Outline each Trypanosoma brucei.
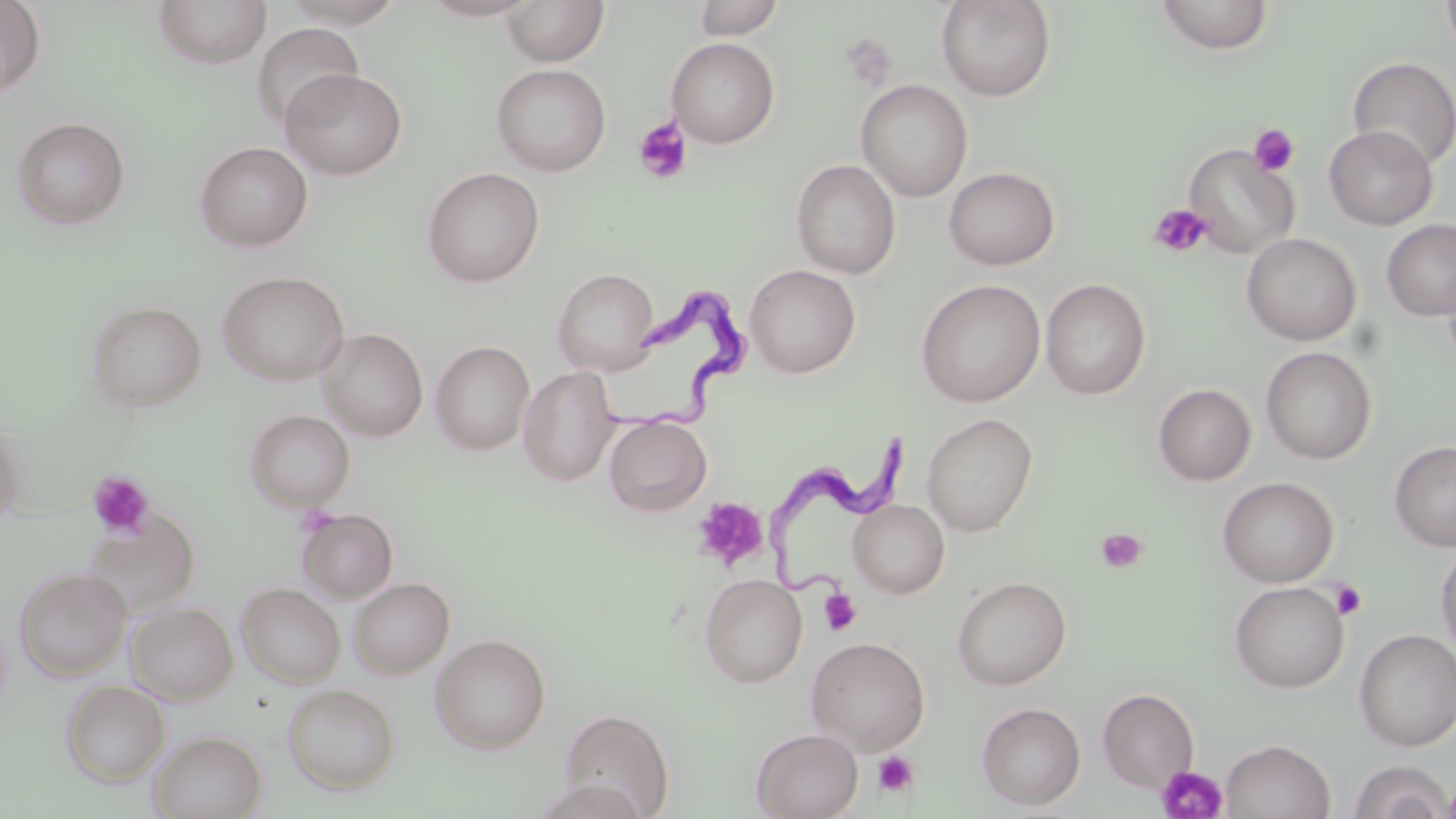

Approximate bounding boxes as [x1, y1, x2, y2] in pixels.
Trypanosoma brucei: [595, 285, 749, 435], [772, 420, 919, 600].

Summary:
  - Uninfected red blood cell locations: [0, 0, 45, 96], [152, 0, 272, 69], [280, 0, 408, 28], [421, 0, 540, 21], [691, 0, 786, 40], [936, 0, 1057, 102], [1154, 0, 1274, 55], [1440, 0, 1456, 57], [502, 1, 609, 67], [251, 23, 364, 130], [666, 37, 780, 148], [1347, 56, 1456, 169], [491, 63, 611, 176], [280, 68, 407, 180], [855, 80, 973, 202], [11, 116, 131, 229], [1323, 125, 1437, 230], [194, 141, 313, 251], [1182, 144, 1299, 259], [791, 159, 901, 279], [943, 166, 1060, 270], [422, 167, 545, 288], [1381, 219, 1456, 321], [1242, 233, 1361, 345], [745, 264, 861, 379], [1441, 267, 1456, 372], [551, 268, 660, 375], [217, 270, 349, 386], [1041, 278, 1151, 399], [916, 280, 1045, 407], [85, 300, 207, 411], [319, 328, 428, 441], [430, 340, 535, 455], [1260, 346, 1377, 464], [519, 366, 619, 486], [1152, 383, 1256, 485], [244, 409, 355, 512], [920, 413, 1038, 536], [604, 416, 712, 517], [0, 422, 23, 525], [1389, 440, 1456, 552], [1217, 476, 1339, 587], [848, 499, 949, 598], [297, 507, 398, 603], [82, 508, 201, 616], [1435, 542, 1456, 661], [15, 568, 131, 681], [699, 573, 808, 688], [952, 576, 1072, 690], [348, 577, 454, 679], [1229, 581, 1349, 693], [236, 582, 346, 688], [126, 601, 238, 704], [1354, 629, 1456, 751], [430, 633, 551, 754], [806, 636, 930, 754], [61, 680, 169, 786], [282, 683, 400, 797], [1097, 688, 1200, 791], [976, 702, 1086, 810], [559, 708, 674, 818], [751, 728, 863, 819], [149, 731, 267, 819], [1221, 738, 1335, 819], [1348, 759, 1453, 819]
  - Platelet locations: [839, 33, 896, 90], [633, 118, 692, 185], [1248, 124, 1300, 177], [1149, 203, 1213, 258], [87, 471, 155, 540], [693, 497, 768, 571], [1095, 528, 1146, 573], [1331, 580, 1368, 621], [819, 589, 861, 636], [872, 750, 920, 799], [1154, 764, 1228, 819]
  - Slide-level diagnosis: Trypanosoma brucei
  - Preparation: thin blood film
  - Modality: light microscopy
  - Field of view: one of a larger specimen
  - Stain: May-Grünwald-Giemsa
  - Image size: 1456×819 pixels
  - Magnification: 1000x